Assess the background quality.
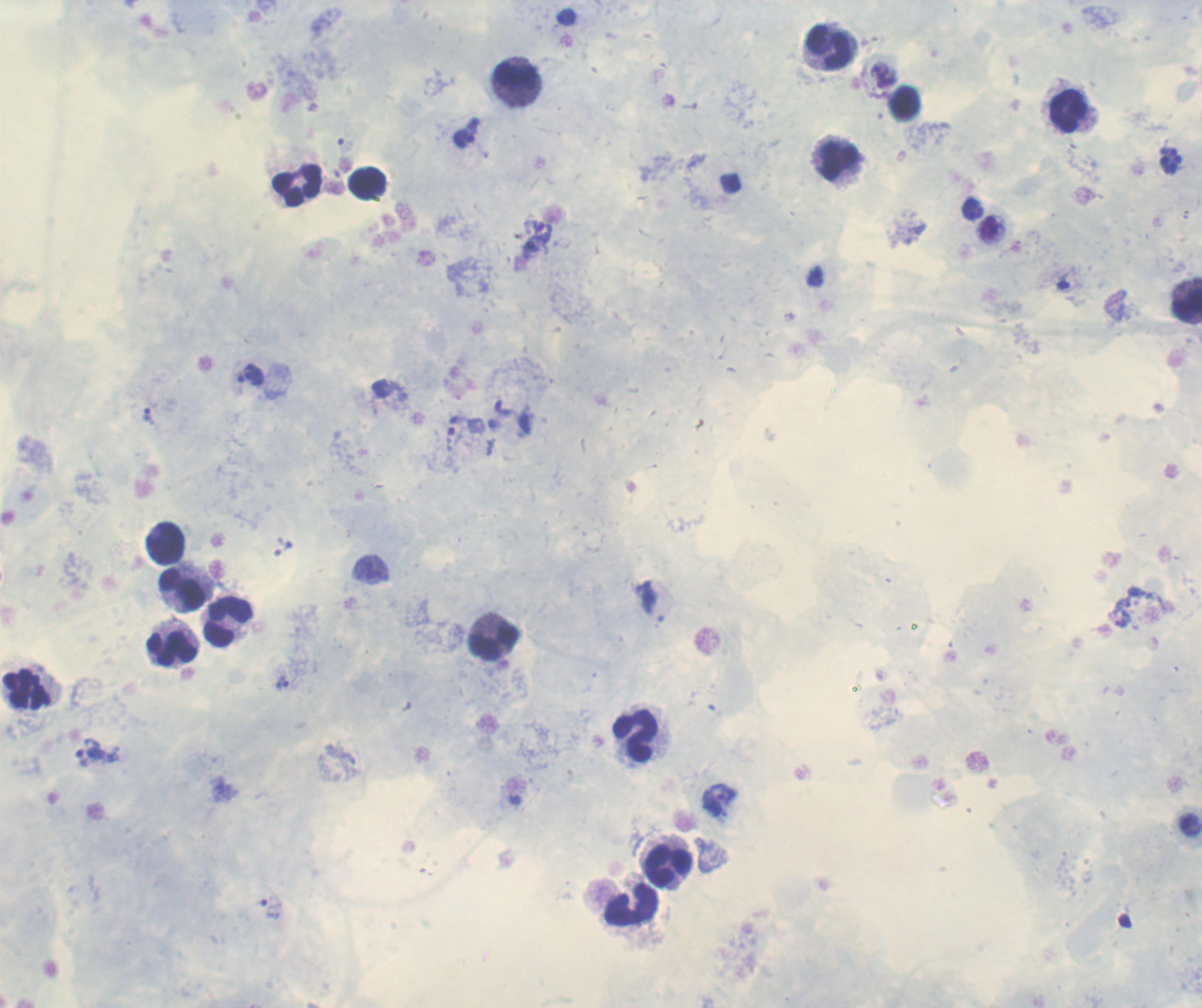
It is good.

Approximate centers as (x, y) in pixels. Leukocyte locations: (830, 47), (515, 82), (904, 102), (1066, 111), (837, 161), (298, 183), (368, 183), (1187, 300), (163, 543), (182, 588), (228, 620), (493, 637), (174, 648), (26, 690), (637, 735), (669, 866), (630, 905). Trophozoite locations: (463, 138), (973, 209), (991, 229), (1063, 284), (255, 373), (239, 384), (148, 416), (1127, 596), (650, 597), (1119, 618), (282, 684), (87, 752), (718, 800), (269, 909). Previously used in a real diagnosis. Result: malaria parasites identified. Thick blood smear. Romanowsky stain. Coloration quality: good. Captured at 100x magnification. Image is 1202×1008 pixels. One field from this slide.